Report the malaria status of this cell.
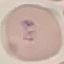

Parasitized.

Photographed with a smartphone camera at the microscope eyepiece. Giemsa-stained preparation. Cell patch, automatically extracted from a larger field of view and resized to 64 × 64 pixels. Thin blood smear.